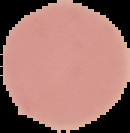
Summary:
  - Malaria status: uninfected
  - Preparation: thin blood film
  - Image type: segmented cell region on a black background
  - Image size: 130×133 pixels